Report the malaria status of this cell.
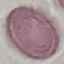
Uninfected.

Summary:
  - Capture: smartphone camera at the microscope eyepiece
  - Image type: cell patch, automatically extracted from a larger field of view and resized to 64 × 64 pixels
  - Preparation: thin blood film
  - Stain: Giemsa